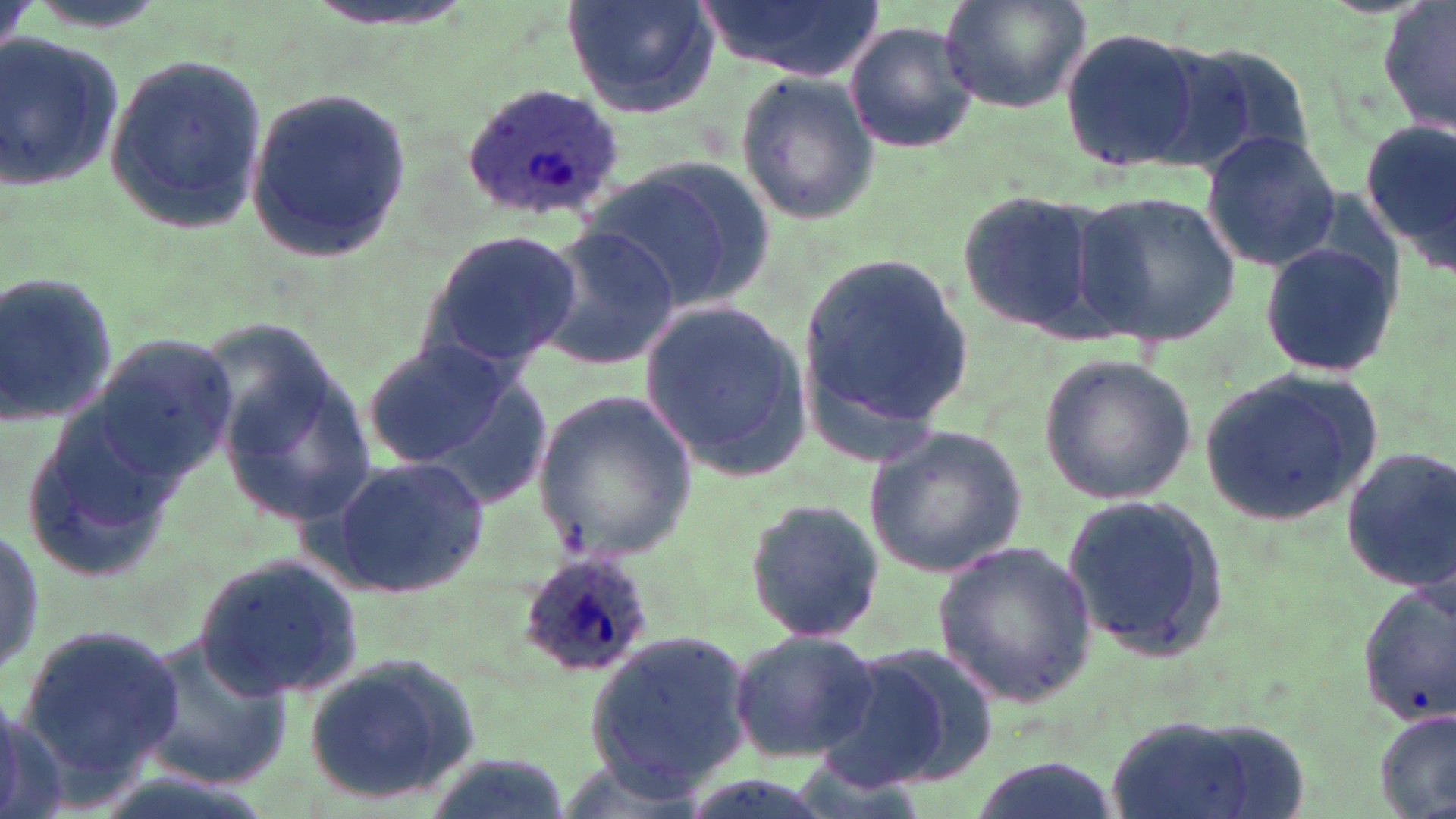

{
  "slide_level_diagnosis": "Plasmodium ovale",
  "modality": "light microscopy",
  "stain": "May-Grünwald-Giemsa",
  "magnification": "1000x",
  "preparation": "thin blood film",
  "plasmodium_ovale_infected_red_blood_cell_locations": "approximate bounding boxes as named x1/y1/x2/y2 corners in pixels: (x1=462, y1=82, x2=625, y2=221), (x1=514, y1=551, x2=659, y2=683)",
  "uninfected_red_blood_cell_locations": "approximate bounding boxes as named x1/y1/x2/y2 corners in pixels: (x1=304, y1=0, x2=478, y2=33), (x1=561, y1=0, x2=718, y2=118), (x1=698, y1=0, x2=884, y2=79), (x1=940, y1=0, x2=1091, y2=116), (x1=1381, y1=0, x2=1456, y2=139), (x1=842, y1=21, x2=977, y2=155), (x1=1061, y1=25, x2=1213, y2=173), (x1=1, y1=30, x2=122, y2=189), (x1=1164, y1=35, x2=1318, y2=175), (x1=105, y1=52, x2=266, y2=235), (x1=734, y1=70, x2=882, y2=224), (x1=245, y1=86, x2=410, y2=264), (x1=1360, y1=119, x2=1456, y2=266), (x1=1201, y1=129, x2=1341, y2=271), (x1=588, y1=157, x2=769, y2=313), (x1=957, y1=188, x2=1110, y2=338), (x1=1073, y1=190, x2=1240, y2=347), (x1=531, y1=227, x2=679, y2=369), (x1=416, y1=228, x2=582, y2=377), (x1=1259, y1=239, x2=1399, y2=379), (x1=798, y1=250, x2=975, y2=449), (x1=0, y1=271, x2=117, y2=432), (x1=640, y1=298, x2=812, y2=482), (x1=84, y1=334, x2=237, y2=492), (x1=362, y1=338, x2=517, y2=470), (x1=215, y1=348, x2=378, y2=535), (x1=1039, y1=355, x2=1195, y2=505), (x1=1197, y1=369, x2=1385, y2=524), (x1=533, y1=387, x2=698, y2=564), (x1=19, y1=396, x2=186, y2=580), (x1=862, y1=423, x2=1029, y2=579), (x1=1341, y1=448, x2=1454, y2=590), (x1=324, y1=454, x2=488, y2=599), (x1=1061, y1=491, x2=1229, y2=663), (x1=741, y1=494, x2=887, y2=647), (x1=0, y1=517, x2=45, y2=690), (x1=933, y1=541, x2=1099, y2=705), (x1=197, y1=554, x2=362, y2=701), (x1=1351, y1=582, x2=1455, y2=723), (x1=14, y1=625, x2=186, y2=787), (x1=584, y1=628, x2=755, y2=793), (x1=727, y1=629, x2=879, y2=760), (x1=137, y1=632, x2=294, y2=787), (x1=825, y1=642, x2=999, y2=792), (x1=301, y1=655, x2=482, y2=806), (x1=1376, y1=706, x2=1455, y2=818), (x1=1096, y1=710, x2=1304, y2=819), (x1=423, y1=750, x2=569, y2=819), (x1=964, y1=753, x2=1121, y2=819)",
  "image_size": "1456×819 pixels",
  "field_of_view": "one of a larger specimen"
}